Assess the background quality.
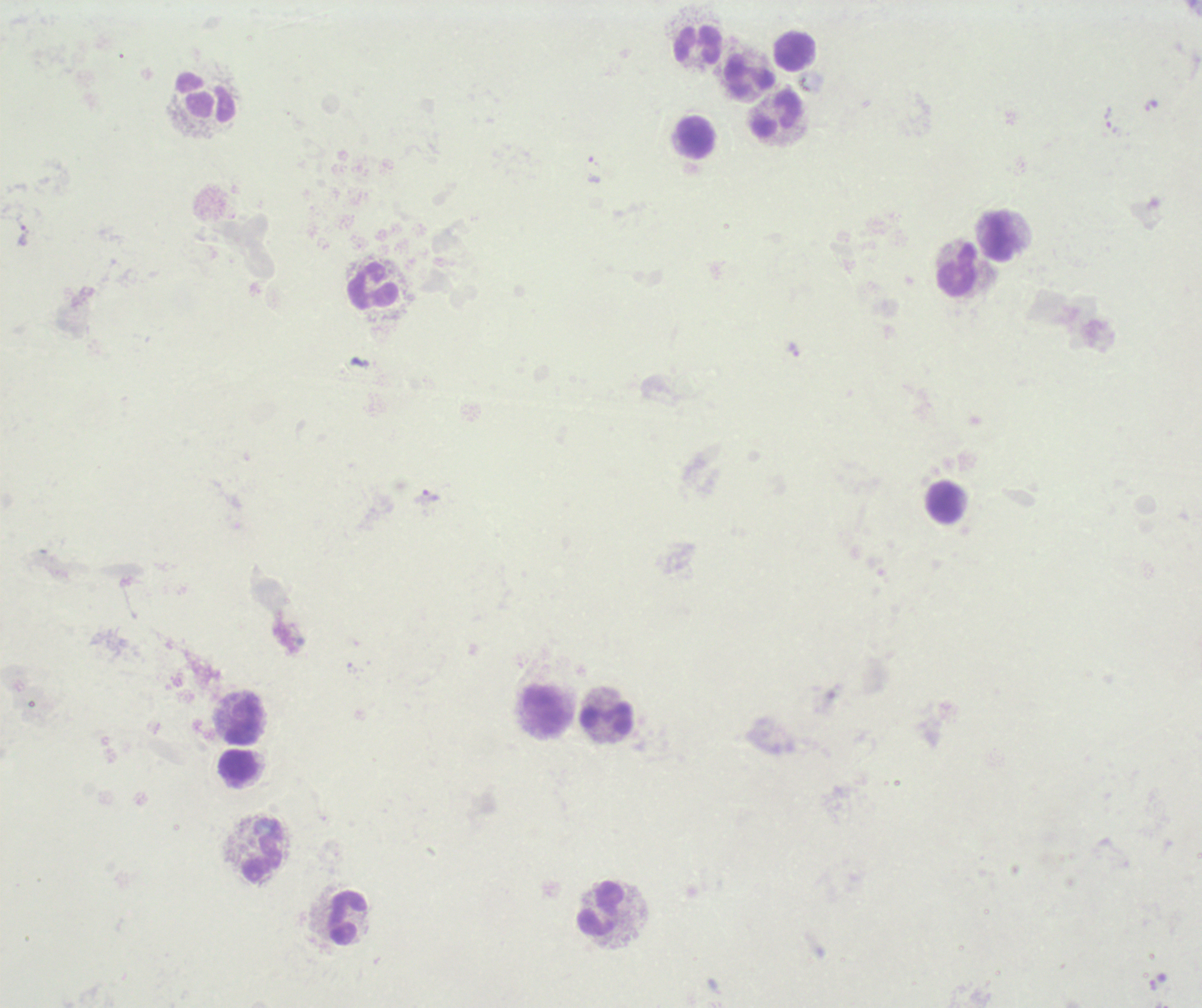
Poor.

Approximate object centers, in pixels from the top-left corner. Leukocyte locations: (x=698, y=44), (x=795, y=51), (x=750, y=77), (x=206, y=99), (x=777, y=112), (x=695, y=137), (x=999, y=236), (x=958, y=269), (x=374, y=287), (x=946, y=502), (x=546, y=711), (x=245, y=717), (x=606, y=717), (x=238, y=765), (x=264, y=851), (x=600, y=908), (x=348, y=917). Trophozoite locations: (x=1110, y=121), (x=24, y=235), (x=794, y=351), (x=426, y=497). Captured at 100x magnification. Image is 1202×1008 pixels. Previously used in an actual diagnosis. Thick blood smear. Romanowsky-stained preparation. One field from this slide. Result: positive for Plasmodium parasites.